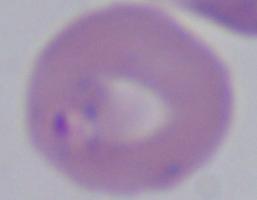

Summary:
  - Identification: Babesia
  - Magnification: 1000x
  - Modality: micrograph